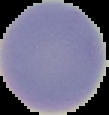

Image is 109×115 pixels. Segmented cell region on a black background. Malaria status: uninfected. From a thin blood film.